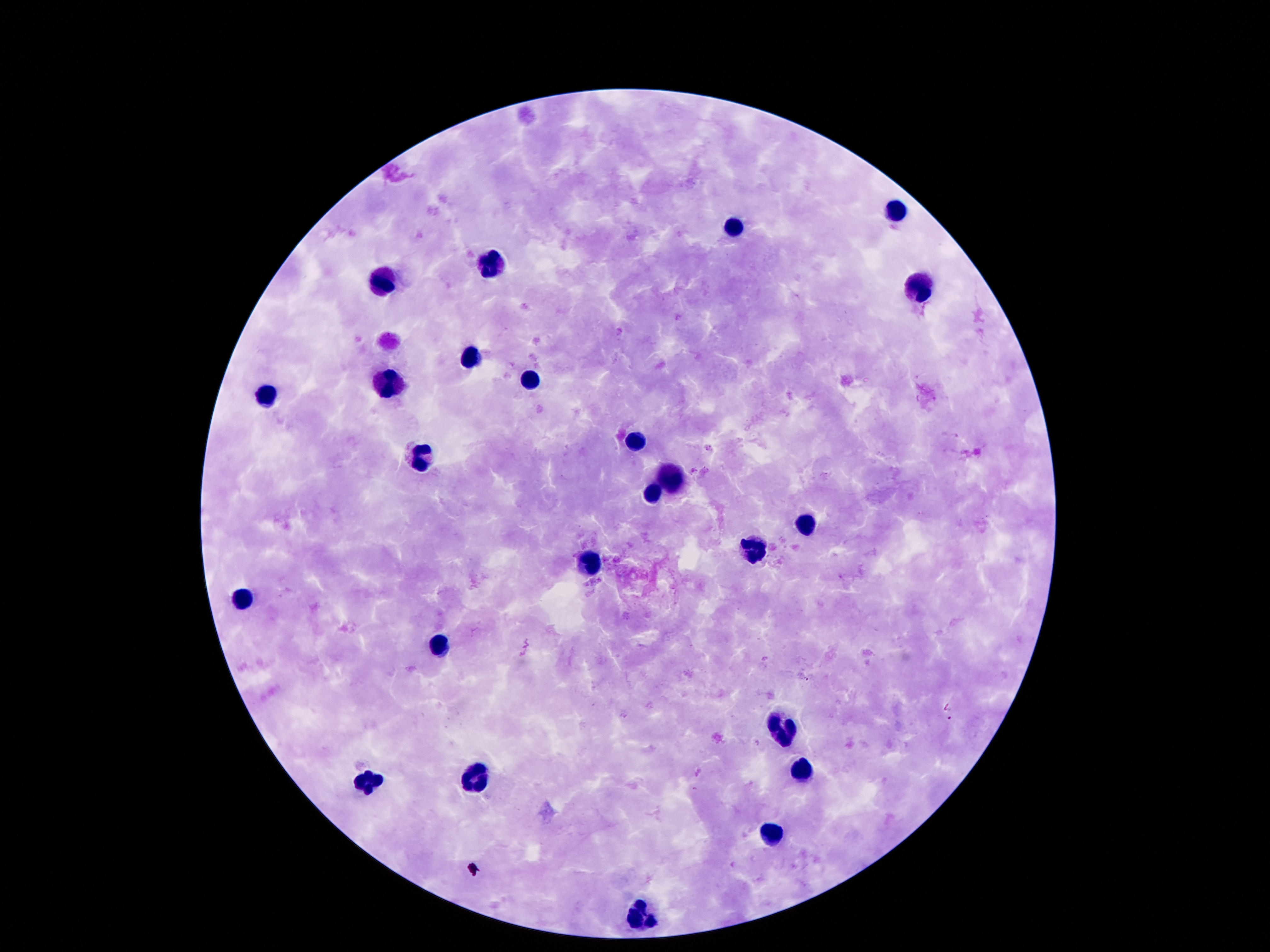

Approximate object centers, in pixels from the top-left corner.
Summary:
  - Leukocyte locations: (x=890, y=212), (x=732, y=228), (x=492, y=263), (x=383, y=282), (x=919, y=290), (x=470, y=357), (x=531, y=379), (x=390, y=384), (x=260, y=394), (x=635, y=443), (x=420, y=455), (x=672, y=479), (x=650, y=492), (x=803, y=527), (x=756, y=552), (x=591, y=566), (x=240, y=596), (x=437, y=646), (x=779, y=728), (x=801, y=770), (x=477, y=780), (x=366, y=785), (x=771, y=836), (x=640, y=921)
  - Magnification: 100x
  - Field of view: one from this slide
  - Stain: Giemsa
  - Capture: smartphone camera through the microscope eyepiece
  - Image size: 1270×952 pixels
  - Patient malaria status: negative
  - Preparation: thick peripheral-blood smear